Assess this cell for malaria.
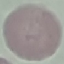

Uninfected.

Cell patch, automatically extracted from a larger field of view and resized to 64 × 64 pixels. Acquired by smartphone through the microscope eyepiece. Thin smear of blood. Giemsa stain.